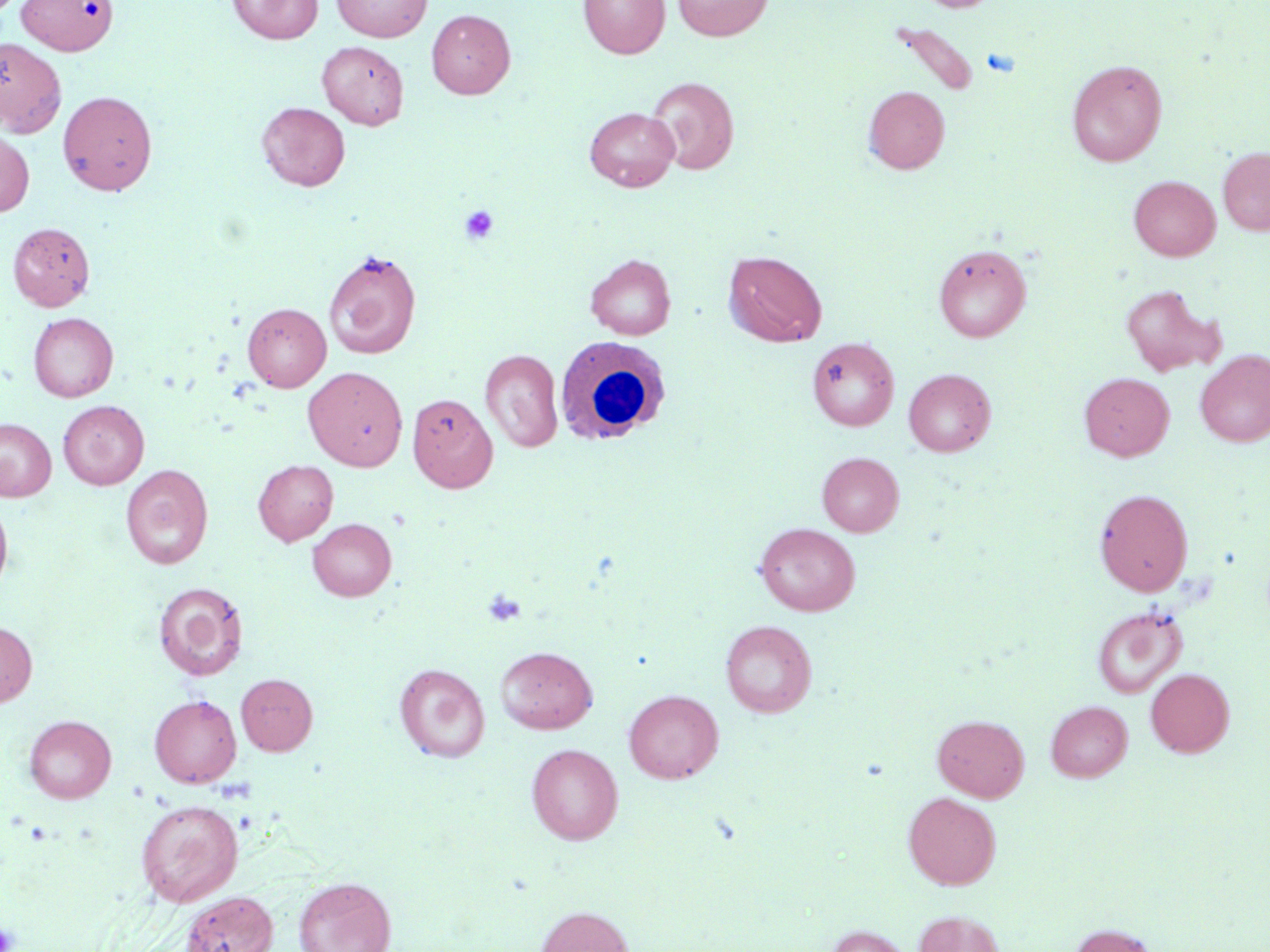 Approximate bounding boxes as (x1, y1, x2, y2) in pixels. White blood cell locations: (555, 337, 670, 445). Uninfected red blood cell locations: (227, 0, 323, 44), (331, 0, 432, 41), (579, 0, 669, 58), (672, 0, 773, 41), (917, 0, 999, 12), (14, 1, 123, 58), (426, 9, 515, 98), (888, 21, 981, 98), (0, 38, 66, 138), (317, 41, 409, 130), (1067, 59, 1167, 166), (646, 76, 739, 174), (864, 86, 950, 174), (58, 90, 158, 196), (256, 101, 350, 191), (584, 106, 680, 191), (0, 129, 34, 217), (1218, 147, 1270, 235), (1129, 175, 1220, 261), (8, 222, 95, 310), (933, 243, 1031, 342), (323, 249, 422, 359), (723, 250, 827, 347), (586, 254, 676, 339), (1120, 284, 1225, 377), (243, 302, 331, 391), (28, 312, 118, 401), (806, 337, 899, 430), (480, 348, 563, 453), (1195, 349, 1270, 446), (303, 366, 408, 470), (903, 368, 996, 456), (1078, 372, 1175, 461), (408, 393, 498, 493), (58, 400, 149, 489), (0, 418, 56, 501), (818, 452, 904, 536), (253, 459, 338, 545), (121, 464, 213, 570), (1094, 488, 1193, 596), (0, 498, 13, 599), (308, 518, 397, 601), (754, 523, 860, 616), (153, 582, 248, 681), (1092, 606, 1187, 698), (720, 620, 817, 717), (0, 621, 37, 707), (495, 646, 598, 733), (395, 663, 490, 762), (1145, 668, 1234, 757), (236, 673, 318, 755), (624, 689, 723, 783), (149, 695, 241, 787), (1046, 700, 1132, 782), (933, 714, 1029, 801), (24, 715, 116, 803), (526, 743, 623, 845), (903, 791, 1001, 889), (135, 799, 244, 906), (293, 876, 396, 952), (180, 890, 278, 952), (536, 906, 634, 952), (914, 911, 1006, 952), (1070, 924, 1160, 952), (825, 925, 913, 952). Platelet locations: (459, 204, 499, 245), (483, 588, 526, 627), (0, 921, 18, 951). Slide-level diagnosis: negative for blood parasites. One field of a larger specimen. Captured at 1000x magnification. Light microscopy. Thin blood smear. Image is 1270×952 pixels. May-Grünwald-Giemsa-stained preparation.